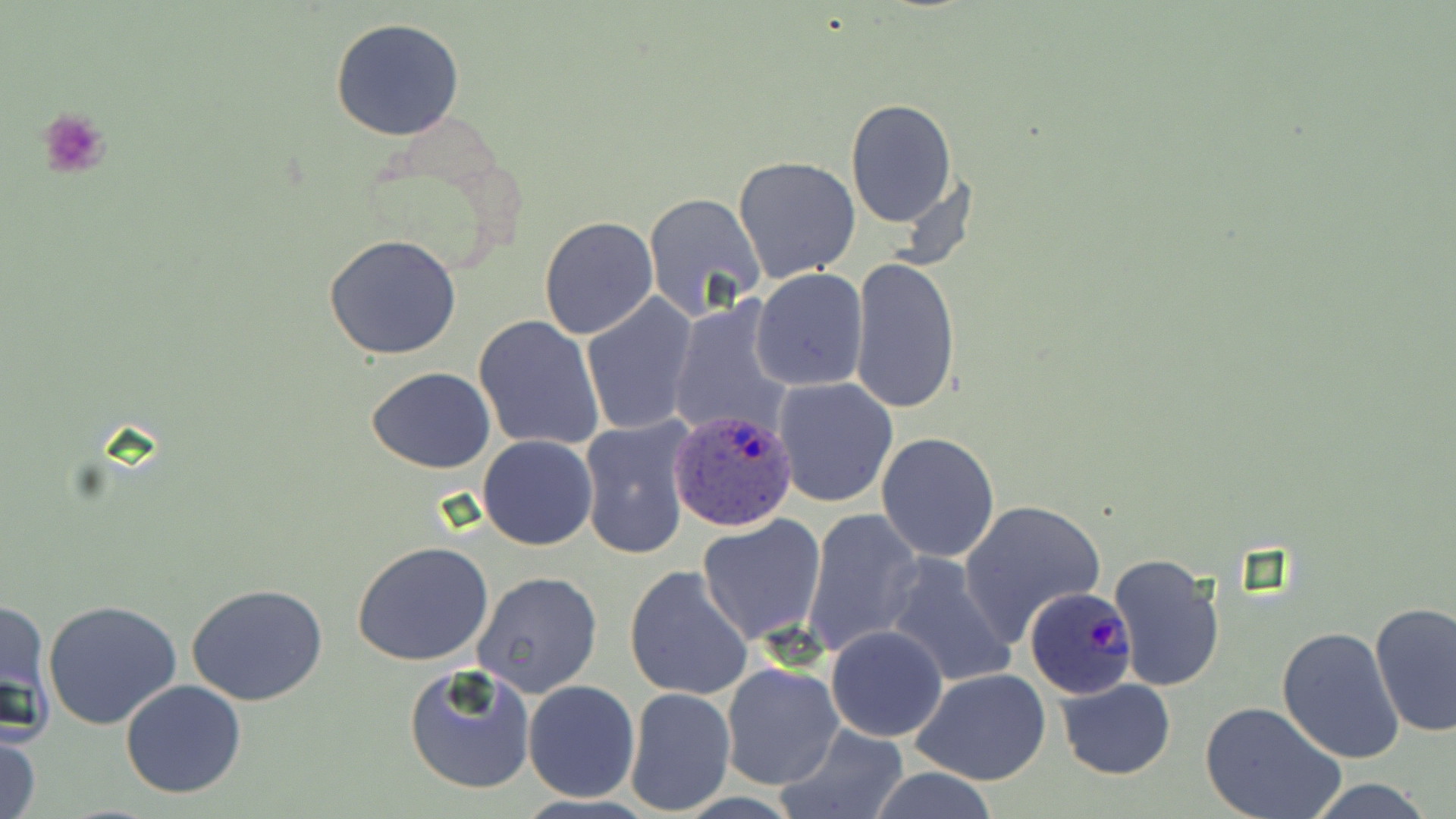

Summary:
  - Coordinate format: approximate bounding boxes as named x1/y1/x2/y2 corners in pixels
  - Platelet locations: (x1=35, y1=106, x2=114, y2=181)
  - Uninfected red blood cell locations: (x1=330, y1=18, x2=465, y2=140), (x1=845, y1=99, x2=958, y2=227), (x1=732, y1=156, x2=860, y2=286), (x1=642, y1=191, x2=766, y2=321), (x1=538, y1=215, x2=659, y2=340), (x1=323, y1=233, x2=463, y2=359), (x1=850, y1=255, x2=961, y2=414), (x1=758, y1=264, x2=883, y2=504), (x1=750, y1=269, x2=869, y2=391), (x1=582, y1=295, x2=699, y2=436), (x1=665, y1=301, x2=797, y2=439), (x1=473, y1=315, x2=604, y2=452), (x1=366, y1=367, x2=495, y2=474), (x1=773, y1=376, x2=899, y2=508), (x1=578, y1=418, x2=693, y2=561), (x1=876, y1=432, x2=1001, y2=561), (x1=478, y1=435, x2=598, y2=549), (x1=958, y1=499, x2=1106, y2=641), (x1=803, y1=509, x2=924, y2=656), (x1=696, y1=515, x2=825, y2=645), (x1=352, y1=542, x2=497, y2=667), (x1=1108, y1=551, x2=1226, y2=694), (x1=884, y1=552, x2=1020, y2=689), (x1=623, y1=565, x2=755, y2=702), (x1=471, y1=571, x2=603, y2=698), (x1=185, y1=582, x2=329, y2=705), (x1=1, y1=597, x2=54, y2=742), (x1=43, y1=599, x2=182, y2=730), (x1=1369, y1=600, x2=1455, y2=739), (x1=825, y1=625, x2=948, y2=741), (x1=1276, y1=627, x2=1406, y2=765), (x1=719, y1=662, x2=844, y2=791), (x1=402, y1=664, x2=534, y2=795), (x1=910, y1=667, x2=1052, y2=786), (x1=120, y1=678, x2=247, y2=800), (x1=1054, y1=678, x2=1176, y2=780), (x1=523, y1=680, x2=640, y2=802), (x1=625, y1=689, x2=736, y2=814), (x1=1200, y1=701, x2=1346, y2=819), (x1=776, y1=725, x2=910, y2=819), (x1=1, y1=731, x2=43, y2=819), (x1=858, y1=767, x2=1005, y2=819), (x1=1298, y1=777, x2=1442, y2=819)
  - Plasmodium ovale-infected red blood cell locations: (x1=667, y1=409, x2=801, y2=534), (x1=1024, y1=585, x2=1139, y2=700)
  - Slide-level diagnosis: Plasmodium ovale
  - Image size: 1456×819 pixels
  - Modality: light microscopy
  - Field of view: single
  - Magnification: 1000x
  - Preparation: thin blood film
  - Stain: May-Grünwald-Giemsa